Name the parasite shown.
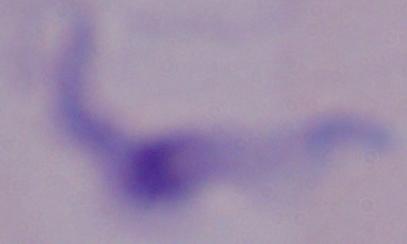

This is a trypanosome.

Captured at 1000x magnification. Micrograph.